Locate every malaria parasite and every leukocyte.
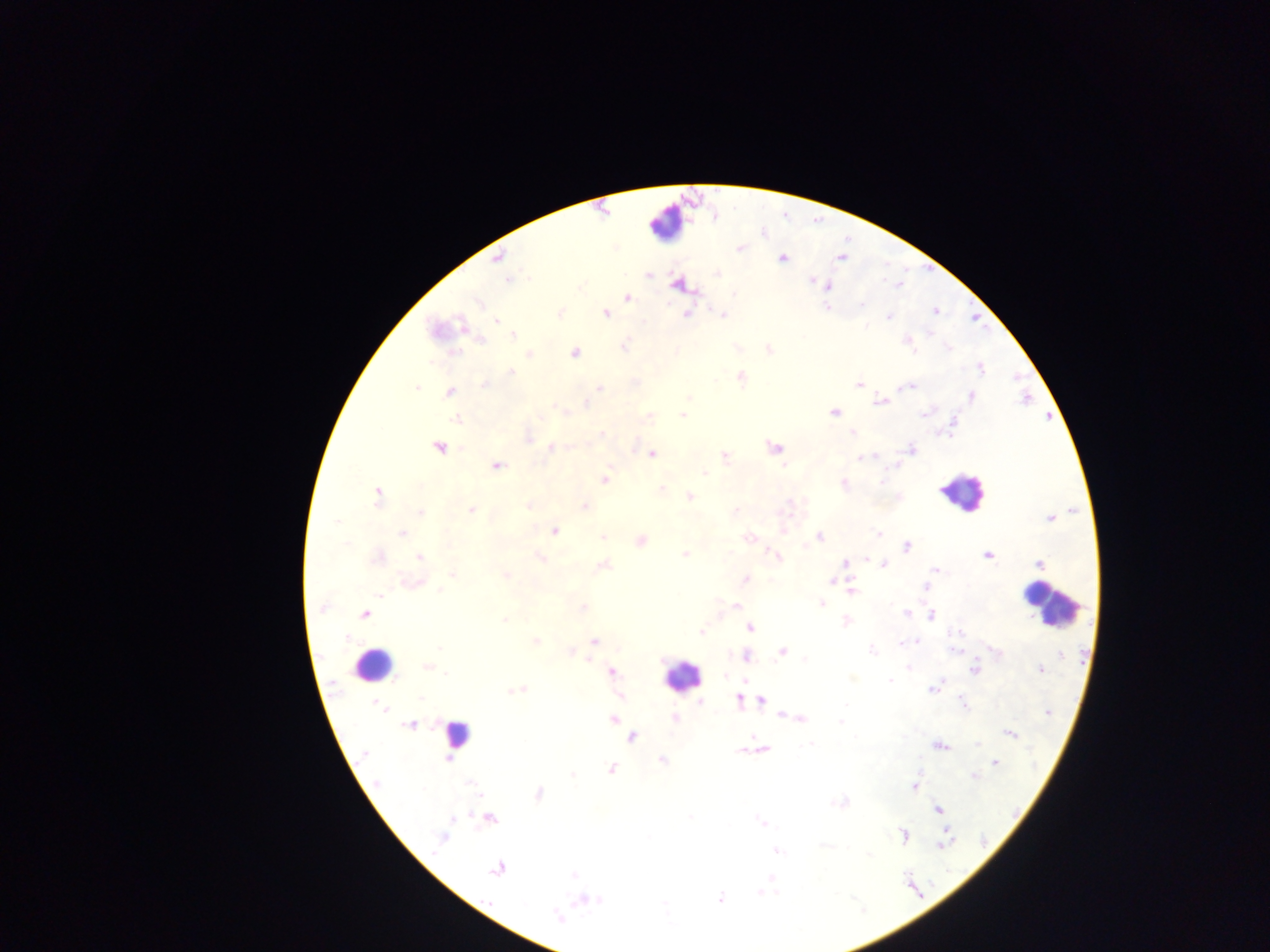
Approximate centers as {x, y} in pixels.
Malaria parasites: {741, 248}, {498, 257}, {841, 257}, {782, 258}, {648, 275}, {508, 279}, {813, 281}, {676, 285}, {828, 286}, {734, 293}, {628, 298}, {477, 303}, {861, 303}, {828, 306}, {935, 311}, {606, 314}, {686, 314}, {723, 315}, {889, 317}, {497, 320}, {867, 327}, {513, 336}, {480, 339}, {907, 343}, {624, 346}, {948, 347}, {769, 349}, {453, 352}, {574, 352}, {528, 353}, {981, 368}, {511, 372}, {741, 377}, {859, 384}, {484, 385}, {417, 387}, {909, 387}, {599, 388}, {449, 392}, {971, 396}, {688, 397}, {879, 402}, {586, 405}, {563, 412}, {834, 413}, {923, 414}, {683, 415}, {649, 416}, {456, 419}, {853, 432}, {601, 434}, {528, 438}, {438, 447}, {551, 447}, {774, 447}, {911, 450}, {652, 454}, {724, 456}, {875, 457}, {860, 458}, {783, 465}, {497, 466}, {705, 473}, {605, 479}, {881, 481}, {843, 484}, {662, 490}, {377, 494}, {688, 496}, {789, 502}, {529, 506}, {585, 506}, {471, 510}, {735, 510}, {420, 512}, {1050, 518}, {338, 522}, {554, 531}, {784, 531}, {402, 533}, {878, 534}, {603, 537}, {749, 538}, {819, 538}, {640, 541}, {907, 547}, {684, 555}, {987, 555}, {419, 557}, {777, 557}, {378, 558}, {540, 558}, {866, 559}, {846, 562}, {1039, 564}, {603, 565}, {884, 565}, {934, 570}, {453, 575}, {505, 575}, {745, 579}, {831, 581}, {411, 583}, {924, 586}, {440, 591}, {851, 591}, {380, 595}, {821, 604}, {735, 605}, {583, 607}, {322, 608}, {907, 613}, {364, 615}, {931, 616}, {504, 620}, {846, 622}, {750, 628}, {700, 632}, {958, 633}, {347, 638}, {593, 640}, {536, 641}, {917, 642}, {901, 643}, {439, 649}, {872, 650}, {782, 651}, {995, 651}, {570, 652}, {746, 656}, {805, 659}, {588, 660}, {908, 667}, {427, 668}, {974, 669}, {1040, 669}, {611, 672}, {445, 673}, {744, 680}, {889, 680}, {933, 689}, {518, 690}, {619, 696}, {420, 699}, {739, 700}, {761, 700}, {700, 702}, {962, 702}, {846, 703}, {377, 704}, {381, 707}, {1047, 713}, {783, 716}, {800, 718}, {612, 719}, {675, 719}, {840, 722}, {410, 725}, {1010, 734}, {632, 737}, {810, 744}, {977, 745}, {940, 746}, {763, 749}, {740, 750}, {364, 753}, {662, 760}, {996, 763}, {611, 768}, {573, 775}, {974, 776}, {377, 783}, {470, 783}, {915, 786}, {538, 794}, {840, 802}, {938, 810}, {691, 817}, {452, 819}, {490, 819}, {761, 822}, {903, 835}, {441, 839}, {945, 842}, {777, 851}, {869, 855}, {497, 869}, {572, 874}, {772, 878}, {759, 893}, {720, 899}, {599, 900}, {582, 901}, {664, 904}, {556, 917}.
Leukocytes: {666, 224}, {962, 492}, {1050, 606}, {373, 663}, {681, 676}, {456, 735}.

Single field of view. Photographed through a microscope with a mobile-phone camera. Image is 1270×952 pixels. Thick blood smear. Collected in Ghana.